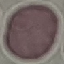
Summary:
  - Malaria status: uninfected
  - Image type: cell patch, automatically extracted from a larger field of view and resized to 64 × 64 pixels
  - Stain: Giemsa
  - Preparation: thin smear
  - Capture: smartphone through the microscope eyepiece